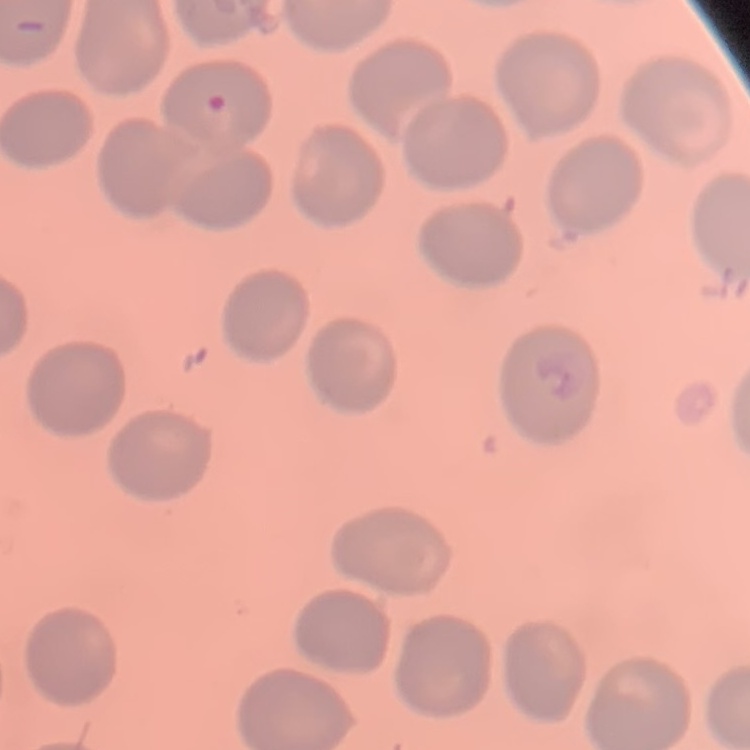

red_blood_cell_morphology: no rouleaux formation
preparation: thin peripheral smear
stain: Field's or Giemsa
image_type: one tile cut from a larger photomicrograph